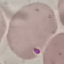

result = malaria parasites detected
image type = automatically extracted cell patch, resized to 64 × 64 pixels
stain = Giemsa
preparation = thin blood smear
capture = smartphone camera at the microscope eyepiece